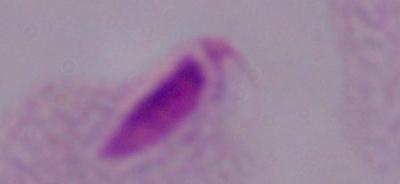

Summary:
  - Identification: trichomonad
  - Magnification: 1000x
  - Modality: micrograph